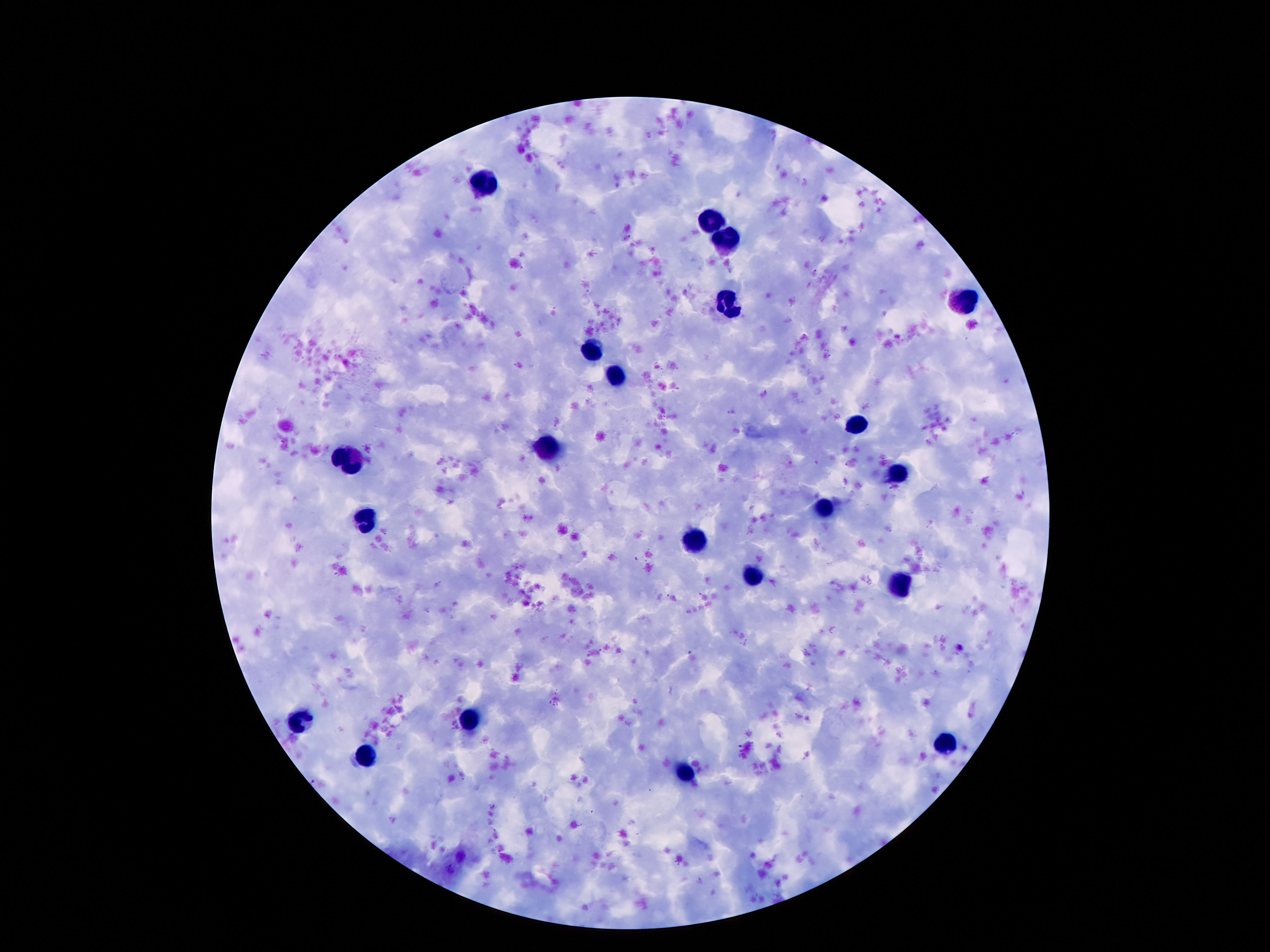

patient malaria status = negative
image size = 1270×952 pixels
stain = Giemsa
leukocyte locations = approximate centers as {x, y} in pixels: {486, 184}, {714, 222}, {729, 244}, {961, 300}, {730, 306}, {593, 348}, {617, 379}, {855, 424}, {548, 450}, {351, 459}, {893, 472}, {824, 507}, {369, 523}, {696, 541}, {752, 573}, {900, 583}, {469, 719}, {298, 720}, {946, 746}, {367, 759}, {687, 773}
magnification = 100x
field of view = single
capture = smartphone camera through the microscope eyepiece
preparation = thick peripheral-blood smear